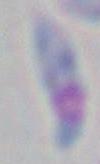
Micrograph. Captured at 1000x magnification. Toxoplasma gondii is shown.